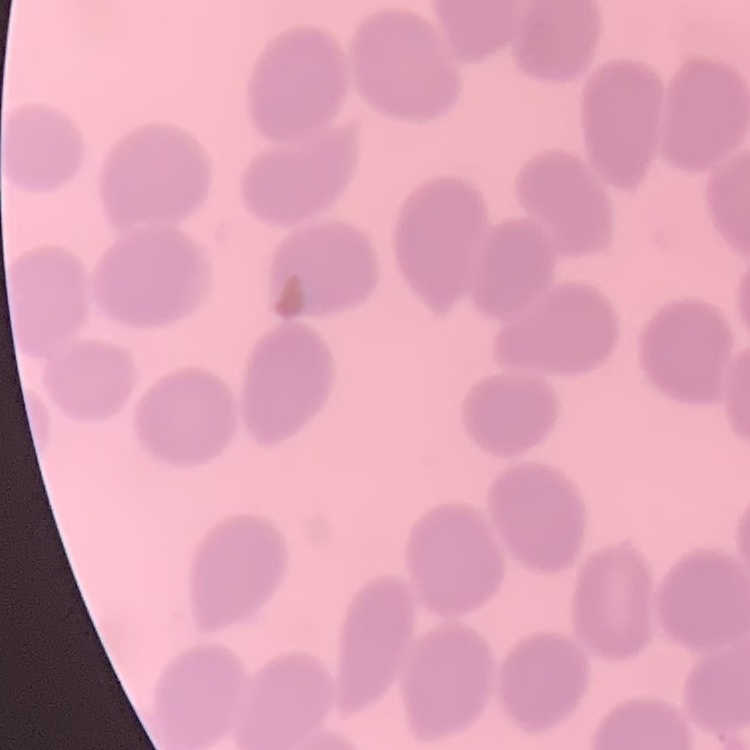

erythrocyte_morphology: no rouleaux formation
preparation: thin peripheral smear
image_type: one tile cut from a larger photomicrograph
stain: Field's or Giemsa